Assess this cell for malaria.
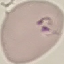

Parasitized.

{
  "stain": "Giemsa",
  "capture": "smartphone camera at the microscope eyepiece",
  "preparation": "thin blood film",
  "image_type": "automatically extracted cell patch, resized to 64 × 64 pixels"
}